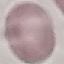
Summary:
  - Result: negative for malaria parasites
  - Capture: smartphone camera at the microscope eyepiece
  - Image type: automatically extracted cell patch, resized to 64 × 64 pixels
  - Stain: Giemsa
  - Preparation: thin blood smear